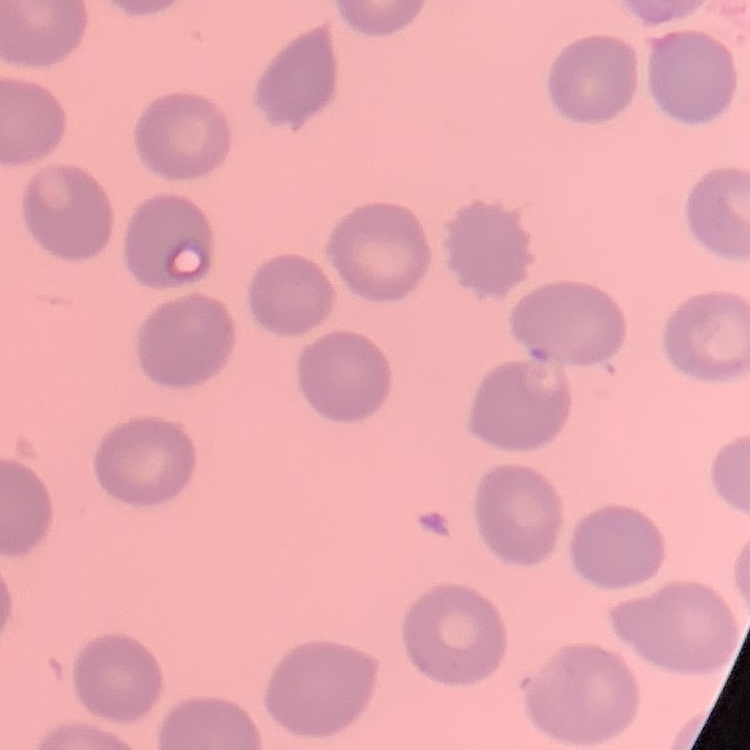

The erythrocytes show no rouleaux formation. One tile cut from a larger photomicrograph. Stained with either Field's or Giemsa. Thin peripheral smear.